Outline each Plasmodium falciparum-infected red blood cell.
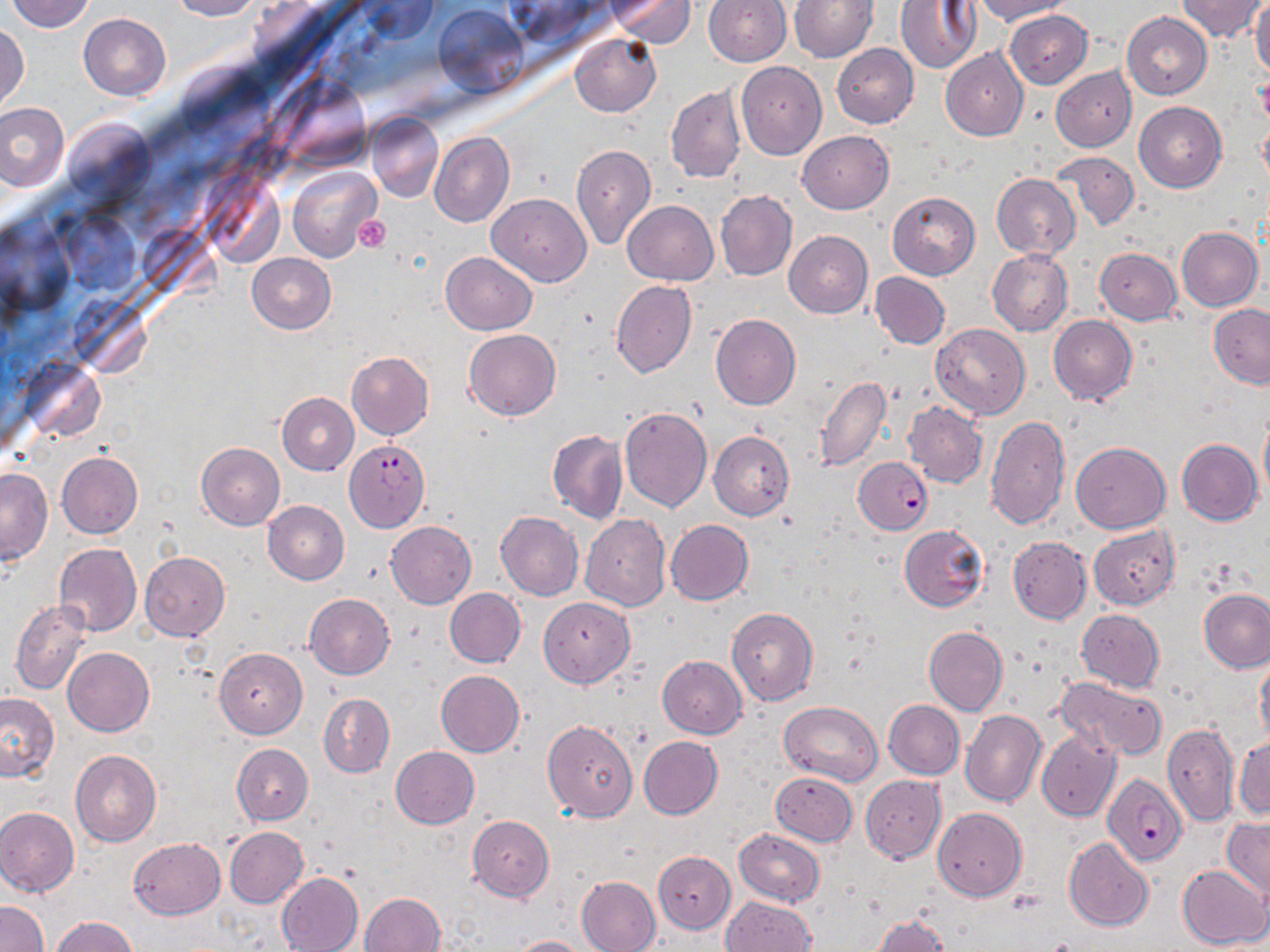
Approximate bounding boxes as named x1/y1/x2/y2 corners in pixels.
Plasmodium falciparum-infected red blood cells: (x1=344, y1=440, x2=430, y2=532), (x1=854, y1=457, x2=932, y2=534), (x1=1102, y1=773, x2=1186, y2=866).

Uninfected red blood cell locations: (x1=4, y1=0, x2=97, y2=33), (x1=169, y1=0, x2=261, y2=20), (x1=360, y1=0, x2=436, y2=45), (x1=608, y1=0, x2=696, y2=45), (x1=704, y1=0, x2=791, y2=66), (x1=790, y1=0, x2=876, y2=62), (x1=896, y1=0, x2=981, y2=73), (x1=973, y1=0, x2=1074, y2=25), (x1=1176, y1=0, x2=1267, y2=43), (x1=1251, y1=2, x2=1270, y2=81), (x1=435, y1=5, x2=527, y2=95), (x1=1005, y1=10, x2=1093, y2=88), (x1=1122, y1=12, x2=1212, y2=99), (x1=78, y1=14, x2=170, y2=101), (x1=0, y1=25, x2=28, y2=116), (x1=570, y1=33, x2=660, y2=117), (x1=832, y1=43, x2=919, y2=128), (x1=941, y1=47, x2=1029, y2=141), (x1=735, y1=61, x2=826, y2=160), (x1=1050, y1=66, x2=1136, y2=152), (x1=666, y1=86, x2=746, y2=183), (x1=0, y1=102, x2=69, y2=191), (x1=1134, y1=102, x2=1226, y2=192), (x1=366, y1=112, x2=443, y2=203), (x1=1257, y1=113, x2=1270, y2=195), (x1=798, y1=131, x2=893, y2=214), (x1=429, y1=132, x2=514, y2=227), (x1=571, y1=144, x2=656, y2=249), (x1=1052, y1=150, x2=1139, y2=230), (x1=289, y1=167, x2=382, y2=263), (x1=991, y1=173, x2=1082, y2=260), (x1=716, y1=190, x2=797, y2=281), (x1=887, y1=191, x2=980, y2=280), (x1=487, y1=193, x2=591, y2=287), (x1=623, y1=200, x2=718, y2=285), (x1=65, y1=214, x2=138, y2=292), (x1=1176, y1=226, x2=1262, y2=311), (x1=784, y1=231, x2=872, y2=318), (x1=1094, y1=248, x2=1182, y2=324), (x1=986, y1=249, x2=1072, y2=336), (x1=441, y1=251, x2=537, y2=335), (x1=246, y1=252, x2=336, y2=334), (x1=869, y1=272, x2=950, y2=350), (x1=612, y1=280, x2=697, y2=378), (x1=1208, y1=304, x2=1270, y2=387), (x1=710, y1=313, x2=801, y2=410), (x1=1048, y1=316, x2=1136, y2=405), (x1=931, y1=323, x2=1029, y2=420), (x1=464, y1=330, x2=560, y2=420), (x1=347, y1=351, x2=433, y2=440), (x1=814, y1=374, x2=893, y2=472), (x1=277, y1=393, x2=359, y2=475), (x1=902, y1=402, x2=988, y2=488), (x1=619, y1=406, x2=712, y2=512), (x1=985, y1=415, x2=1070, y2=530), (x1=1258, y1=416, x2=1270, y2=504), (x1=547, y1=429, x2=627, y2=524), (x1=708, y1=431, x2=794, y2=520), (x1=1176, y1=439, x2=1261, y2=525), (x1=196, y1=442, x2=285, y2=531), (x1=1069, y1=442, x2=1171, y2=533), (x1=56, y1=452, x2=142, y2=539), (x1=0, y1=470, x2=51, y2=562), (x1=262, y1=501, x2=348, y2=585), (x1=495, y1=511, x2=584, y2=600), (x1=581, y1=514, x2=671, y2=611), (x1=665, y1=520, x2=754, y2=605), (x1=386, y1=521, x2=477, y2=609), (x1=897, y1=525, x2=989, y2=612), (x1=1088, y1=525, x2=1180, y2=610), (x1=1007, y1=536, x2=1092, y2=624), (x1=54, y1=543, x2=142, y2=637), (x1=140, y1=552, x2=230, y2=640), (x1=445, y1=588, x2=526, y2=667), (x1=1200, y1=589, x2=1270, y2=672), (x1=304, y1=594, x2=394, y2=680), (x1=538, y1=597, x2=635, y2=687), (x1=10, y1=599, x2=94, y2=695), (x1=727, y1=605, x2=819, y2=706), (x1=1076, y1=609, x2=1165, y2=692), (x1=923, y1=626, x2=1007, y2=716), (x1=62, y1=647, x2=154, y2=737), (x1=215, y1=647, x2=307, y2=738), (x1=1256, y1=653, x2=1270, y2=745), (x1=657, y1=654, x2=747, y2=738), (x1=436, y1=669, x2=524, y2=756), (x1=1055, y1=676, x2=1168, y2=761), (x1=0, y1=691, x2=59, y2=782), (x1=319, y1=693, x2=395, y2=777), (x1=884, y1=700, x2=965, y2=779), (x1=779, y1=701, x2=883, y2=786), (x1=961, y1=710, x2=1047, y2=807), (x1=542, y1=720, x2=638, y2=821), (x1=1162, y1=721, x2=1239, y2=828), (x1=1036, y1=729, x2=1121, y2=822), (x1=1233, y1=734, x2=1270, y2=820), (x1=638, y1=735, x2=722, y2=820), (x1=232, y1=743, x2=313, y2=825), (x1=390, y1=746, x2=480, y2=829), (x1=70, y1=750, x2=161, y2=847), (x1=771, y1=772, x2=857, y2=846), (x1=860, y1=776, x2=945, y2=862), (x1=0, y1=807, x2=79, y2=898), (x1=932, y1=808, x2=1027, y2=900), (x1=467, y1=815, x2=554, y2=902), (x1=1222, y1=817, x2=1270, y2=900), (x1=224, y1=827, x2=308, y2=908), (x1=734, y1=829, x2=826, y2=907), (x1=129, y1=838, x2=226, y2=919), (x1=1064, y1=838, x2=1153, y2=931), (x1=653, y1=852, x2=735, y2=933), (x1=1177, y1=864, x2=1270, y2=950), (x1=276, y1=872, x2=364, y2=952), (x1=576, y1=876, x2=660, y2=952), (x1=359, y1=892, x2=445, y2=952), (x1=721, y1=896, x2=816, y2=952), (x1=0, y1=900, x2=48, y2=952), (x1=873, y1=914, x2=951, y2=952), (x1=52, y1=915, x2=137, y2=951), (x1=508, y1=935, x2=591, y2=952). Platelet locations: (x1=353, y1=214, x2=391, y2=252). Slide-level diagnosis: Plasmodium falciparum. May-Grünwald-Giemsa-stained preparation. Single field of view. Thin blood film. Image is 1270×952 pixels. Light microscopy. 1000x magnification.